Give a bounding box for every leukocyte visible.
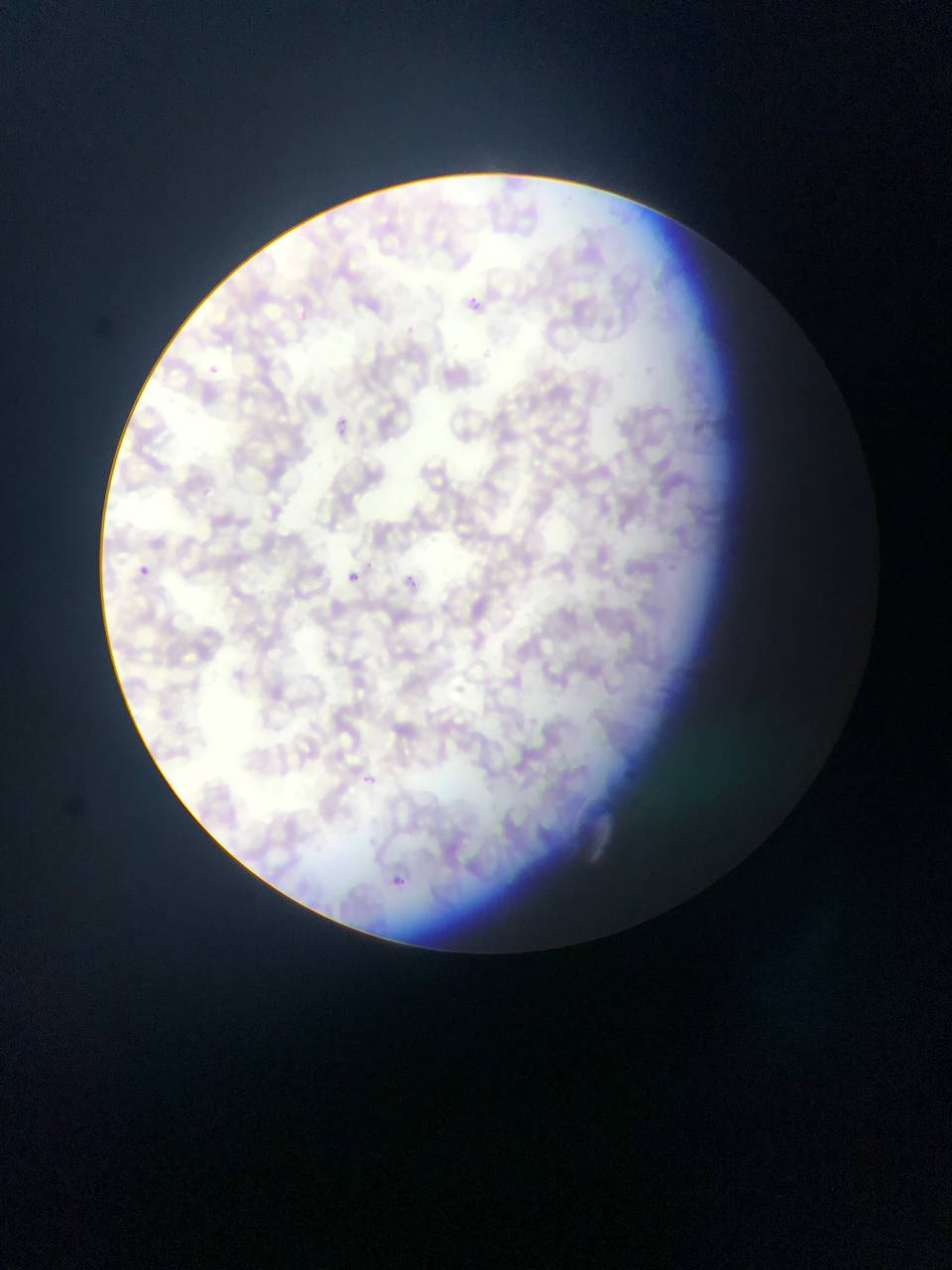
No leukocytes observed.

Approximate bounding boxes as [left, top, right, bottom] in pixels.
Summary:
  - Malaria parasite locations: [466, 293, 478, 311], [202, 362, 224, 380], [333, 416, 350, 436], [134, 563, 152, 580], [344, 571, 358, 584], [404, 575, 418, 588], [360, 772, 378, 789], [382, 870, 412, 895]
  - Country: Ghana
  - Preparation: thin blood film
  - Capture: mobile-phone photograph through a microscope
  - Field of view: single
  - Image size: 952×1270 pixels